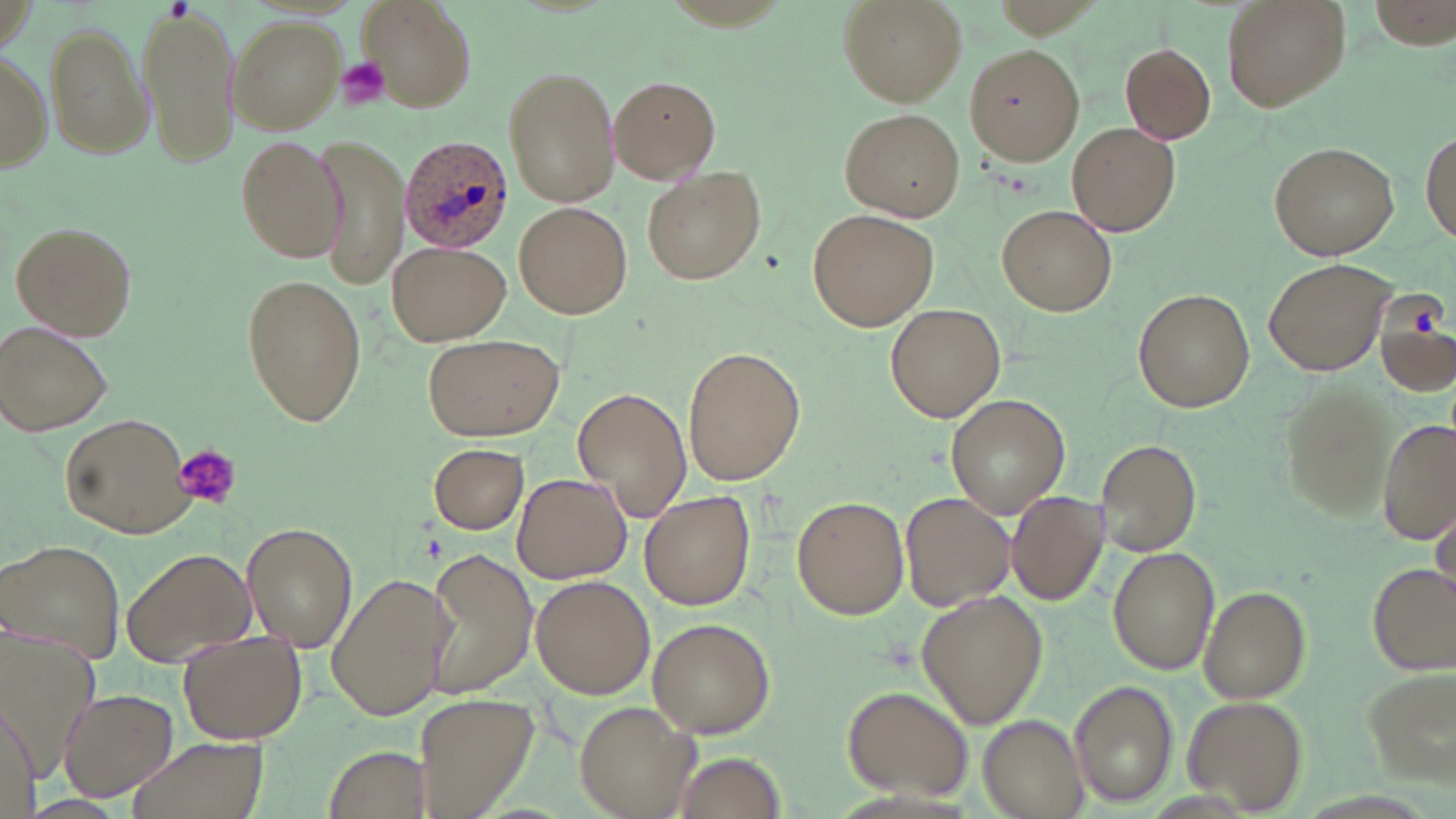
Summary:
  - Coordinate format: approximate bounding boxes as named x1/y1/x2/y2 corners in pixels
  - Plasmodium ovale-infected red blood cell locations: (x1=399, y1=136, x2=514, y2=253)
  - Platelet locations: (x1=337, y1=58, x2=391, y2=110), (x1=171, y1=445, x2=243, y2=509)
  - Uninfected red blood cell locations: (x1=355, y1=0, x2=477, y2=109), (x1=839, y1=0, x2=966, y2=105), (x1=1221, y1=0, x2=1353, y2=113), (x1=1367, y1=0, x2=1455, y2=49), (x1=137, y1=1, x2=243, y2=167), (x1=227, y1=16, x2=345, y2=134), (x1=45, y1=24, x2=152, y2=161), (x1=965, y1=43, x2=1091, y2=165), (x1=1120, y1=43, x2=1216, y2=143), (x1=0, y1=54, x2=51, y2=171), (x1=502, y1=65, x2=622, y2=208), (x1=606, y1=75, x2=721, y2=182), (x1=840, y1=107, x2=966, y2=221), (x1=1068, y1=123, x2=1179, y2=238), (x1=1421, y1=128, x2=1455, y2=246), (x1=233, y1=131, x2=344, y2=263), (x1=315, y1=133, x2=409, y2=290), (x1=1269, y1=142, x2=1400, y2=259), (x1=643, y1=168, x2=764, y2=284), (x1=516, y1=204, x2=631, y2=319), (x1=1000, y1=205, x2=1117, y2=314), (x1=808, y1=209, x2=939, y2=330), (x1=12, y1=221, x2=138, y2=339), (x1=386, y1=241, x2=509, y2=346), (x1=1263, y1=257, x2=1399, y2=376), (x1=240, y1=273, x2=368, y2=425), (x1=1133, y1=288, x2=1255, y2=412), (x1=1374, y1=300, x2=1455, y2=398), (x1=885, y1=303, x2=1006, y2=424), (x1=1, y1=323, x2=114, y2=436), (x1=423, y1=332, x2=564, y2=442), (x1=682, y1=345, x2=805, y2=485), (x1=1278, y1=383, x2=1394, y2=520), (x1=573, y1=388, x2=690, y2=522), (x1=946, y1=395, x2=1070, y2=516), (x1=60, y1=412, x2=196, y2=538), (x1=1379, y1=419, x2=1456, y2=546), (x1=1095, y1=437, x2=1203, y2=554), (x1=428, y1=441, x2=529, y2=534), (x1=512, y1=472, x2=632, y2=583), (x1=640, y1=490, x2=756, y2=611), (x1=901, y1=491, x2=1015, y2=612), (x1=1005, y1=492, x2=1109, y2=607), (x1=793, y1=496, x2=907, y2=619), (x1=1433, y1=501, x2=1456, y2=604), (x1=242, y1=523, x2=357, y2=650), (x1=1, y1=539, x2=127, y2=664), (x1=1108, y1=546, x2=1221, y2=674), (x1=120, y1=547, x2=256, y2=666), (x1=427, y1=549, x2=535, y2=698), (x1=1369, y1=562, x2=1454, y2=671), (x1=326, y1=570, x2=450, y2=723), (x1=530, y1=576, x2=654, y2=698), (x1=1200, y1=586, x2=1311, y2=704), (x1=916, y1=592, x2=1047, y2=729), (x1=648, y1=617, x2=774, y2=737), (x1=177, y1=629, x2=308, y2=743), (x1=1357, y1=663, x2=1454, y2=786), (x1=1068, y1=679, x2=1179, y2=808), (x1=842, y1=686, x2=972, y2=799), (x1=61, y1=690, x2=177, y2=801), (x1=411, y1=692, x2=543, y2=819), (x1=1181, y1=694, x2=1308, y2=812), (x1=574, y1=703, x2=695, y2=819), (x1=0, y1=704, x2=43, y2=817), (x1=975, y1=714, x2=1088, y2=818), (x1=123, y1=733, x2=270, y2=819), (x1=321, y1=742, x2=430, y2=818), (x1=667, y1=750, x2=790, y2=819)
  - Slide-level diagnosis: Plasmodium ovale
  - Image size: 1456×819 pixels
  - Magnification: 1000x
  - Preparation: thin blood film
  - Modality: optical microscopy
  - Field of view: one of a larger specimen
  - Stain: May-Grünwald-Giemsa